Look for Plasmodium parasites.
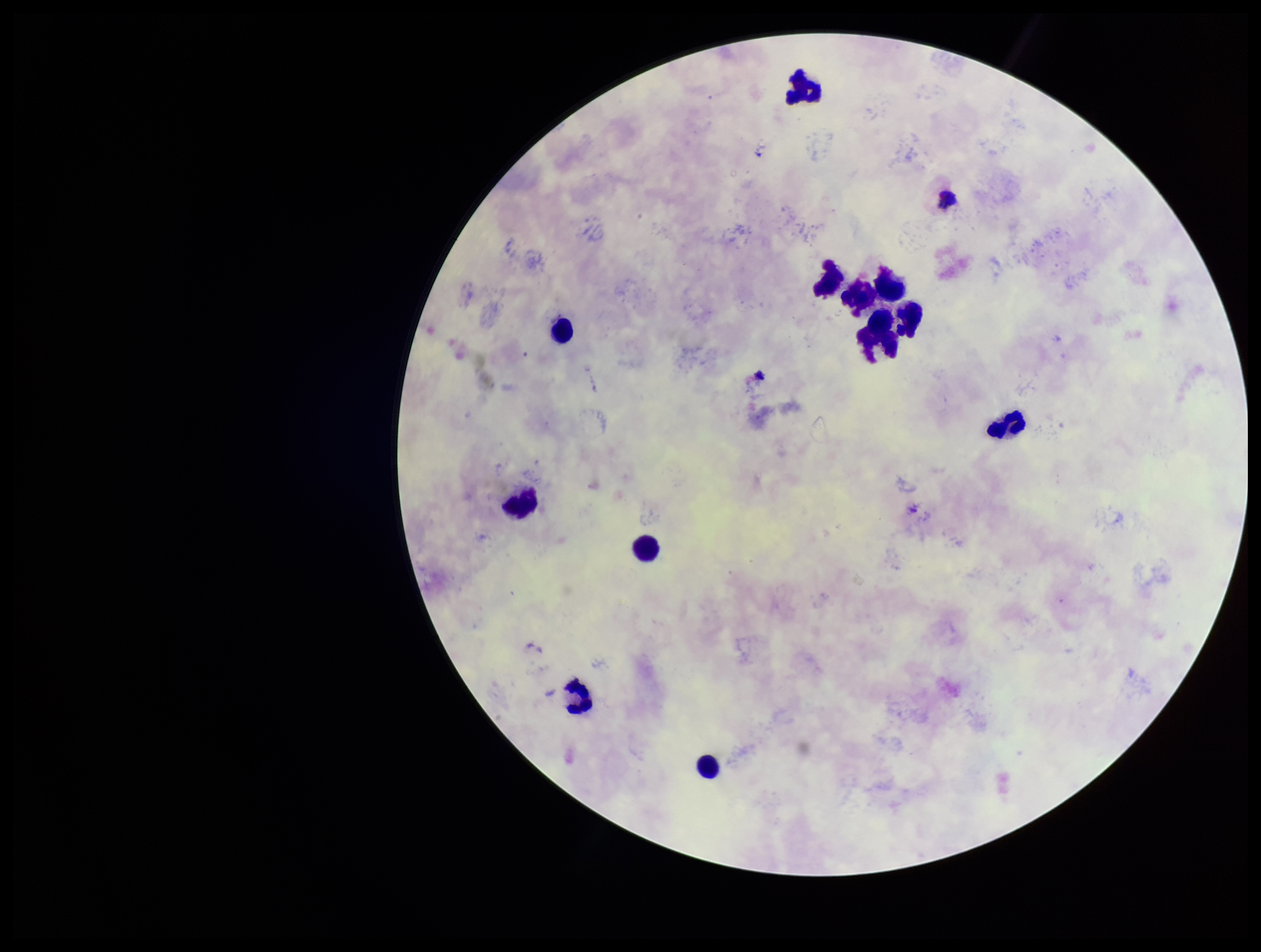
None identified.

{
  "field_of_view": "single",
  "preparation": "thick",
  "patient_malaria_status": "positive",
  "image_size": "1261×952 pixels",
  "stain": "Giemsa",
  "capture": "smartphone photograph through the microscope eyepiece",
  "species_reported_for_this_patient": "Plasmodium vivax",
  "leukocyte_count": 12,
  "parasite_count": 0
}